Assess this cell for malaria.
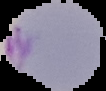

It is parasitized.

image type = segmented cell region with the area outside set to black
image size = 106×91 pixels
preparation = thin blood smear